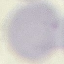

Summary:
  - Result: negative for malaria parasites
  - Capture: smartphone camera at the microscope eyepiece
  - Preparation: thin blood smear
  - Stain: Giemsa
  - Image type: automatically extracted cell patch, resized to 64 × 64 pixels